Give the position of every leukocyte visible.
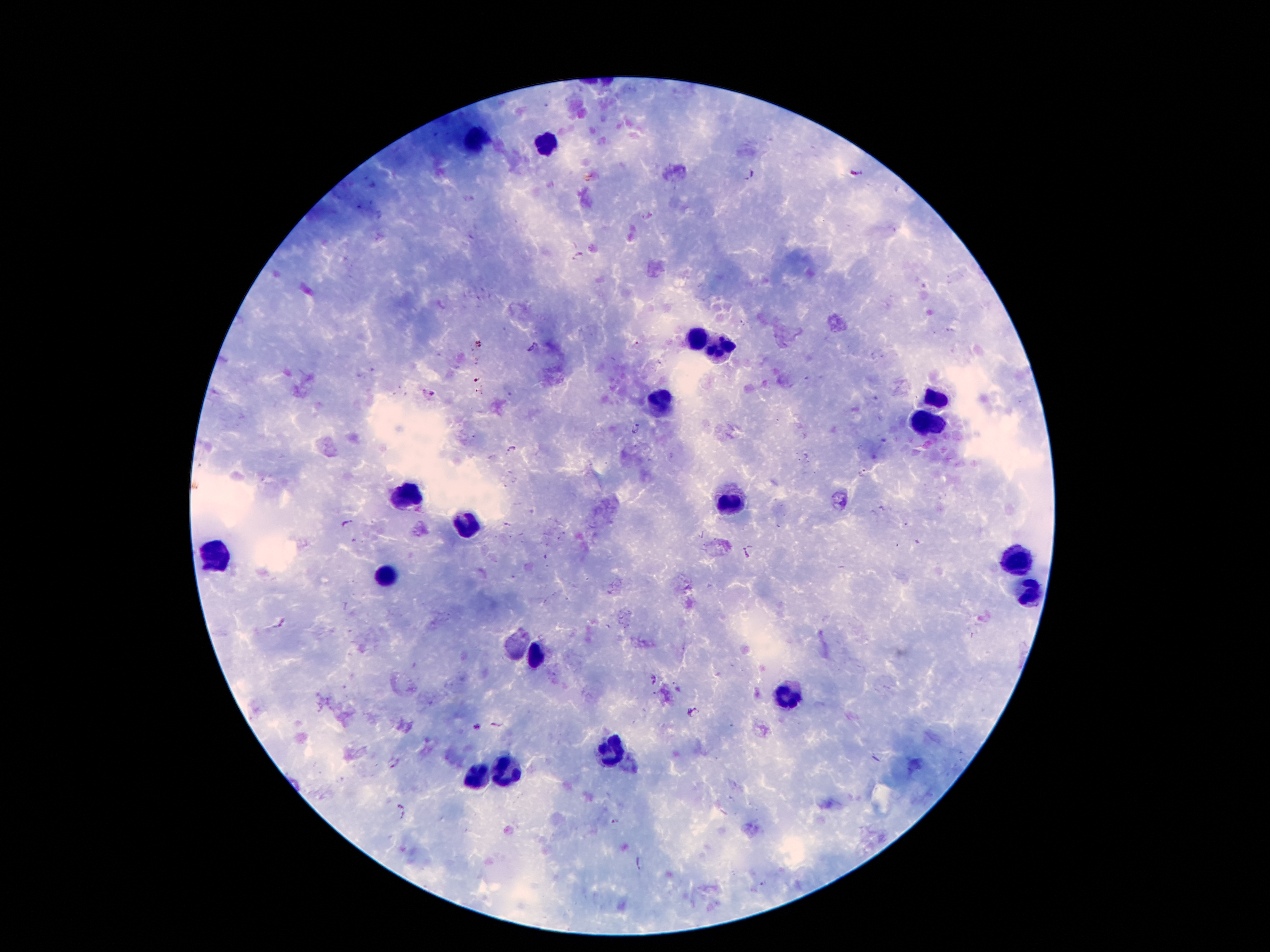
Approximate centers as (x, y) in pixels.
Leukocytes: (481, 143), (546, 145), (697, 334), (716, 346), (935, 397), (662, 403), (930, 422), (403, 495), (733, 504), (462, 527), (216, 552), (1019, 554), (386, 575), (1029, 590), (536, 655), (790, 695), (609, 754), (506, 770), (477, 777).

Plasmodium parasite locations: (749, 174), (577, 254), (532, 347), (635, 430), (509, 448), (862, 472), (348, 523), (745, 553), (654, 679), (693, 711), (478, 727), (394, 762), (402, 813), (617, 821). Giemsa-stained preparation. Patient malaria status: infected with Plasmodium falciparum. 100x magnification. Smartphone photograph taken through the microscope eyepiece. One field from this slide. Image is 1270×952 pixels. Thick blood smear.